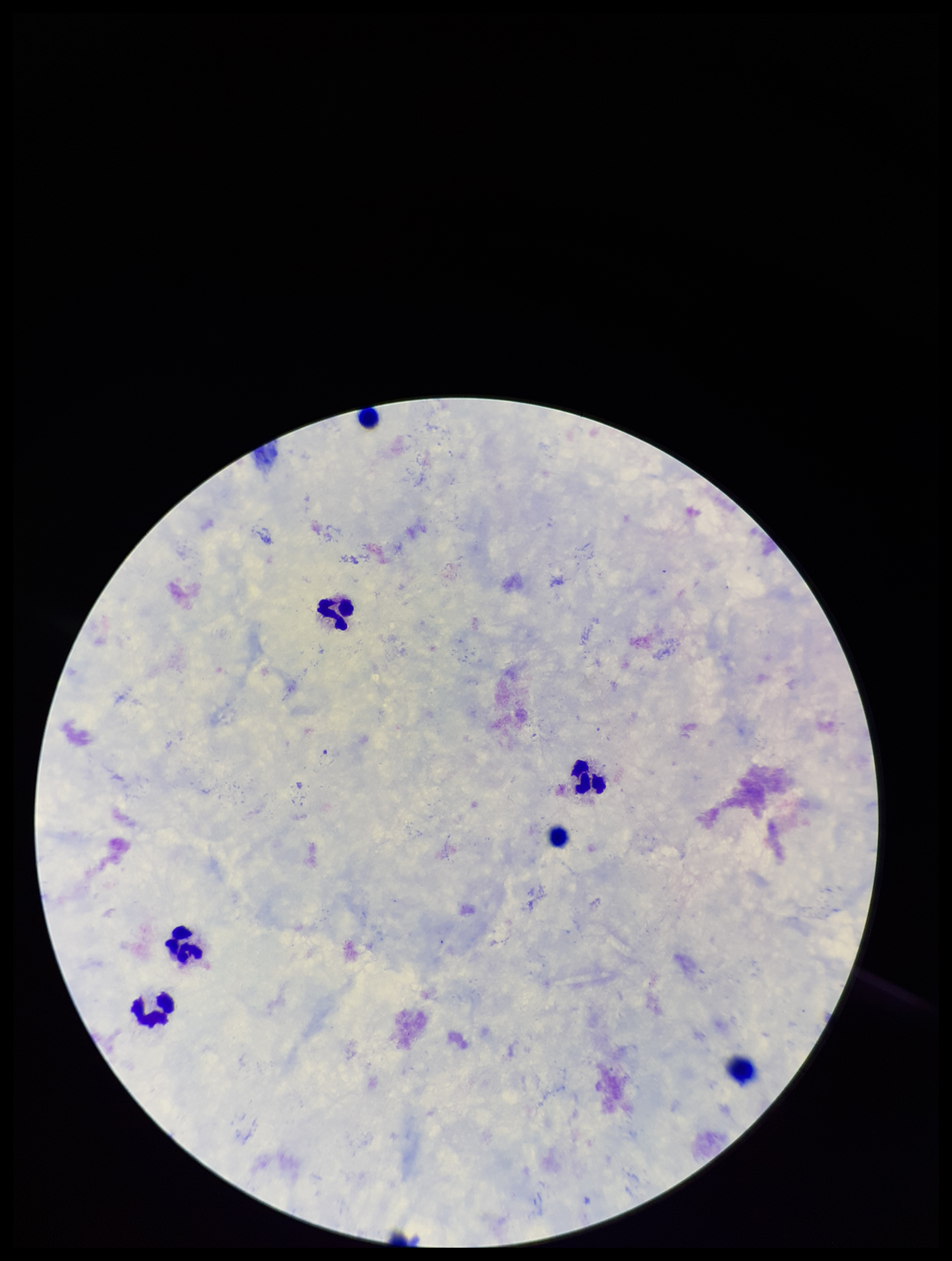

Summary:
  - Parasite count: 0
  - Patient malaria status: negative
  - Stain: Giemsa
  - Image size: 952×1261 pixels
  - Preparation: thick blood smear
  - Plasmodium parasites: none detected
  - Leukocyte count: 7
  - Field of view: single
  - Capture: smartphone photograph through the microscope eyepiece